Give the preparation type.
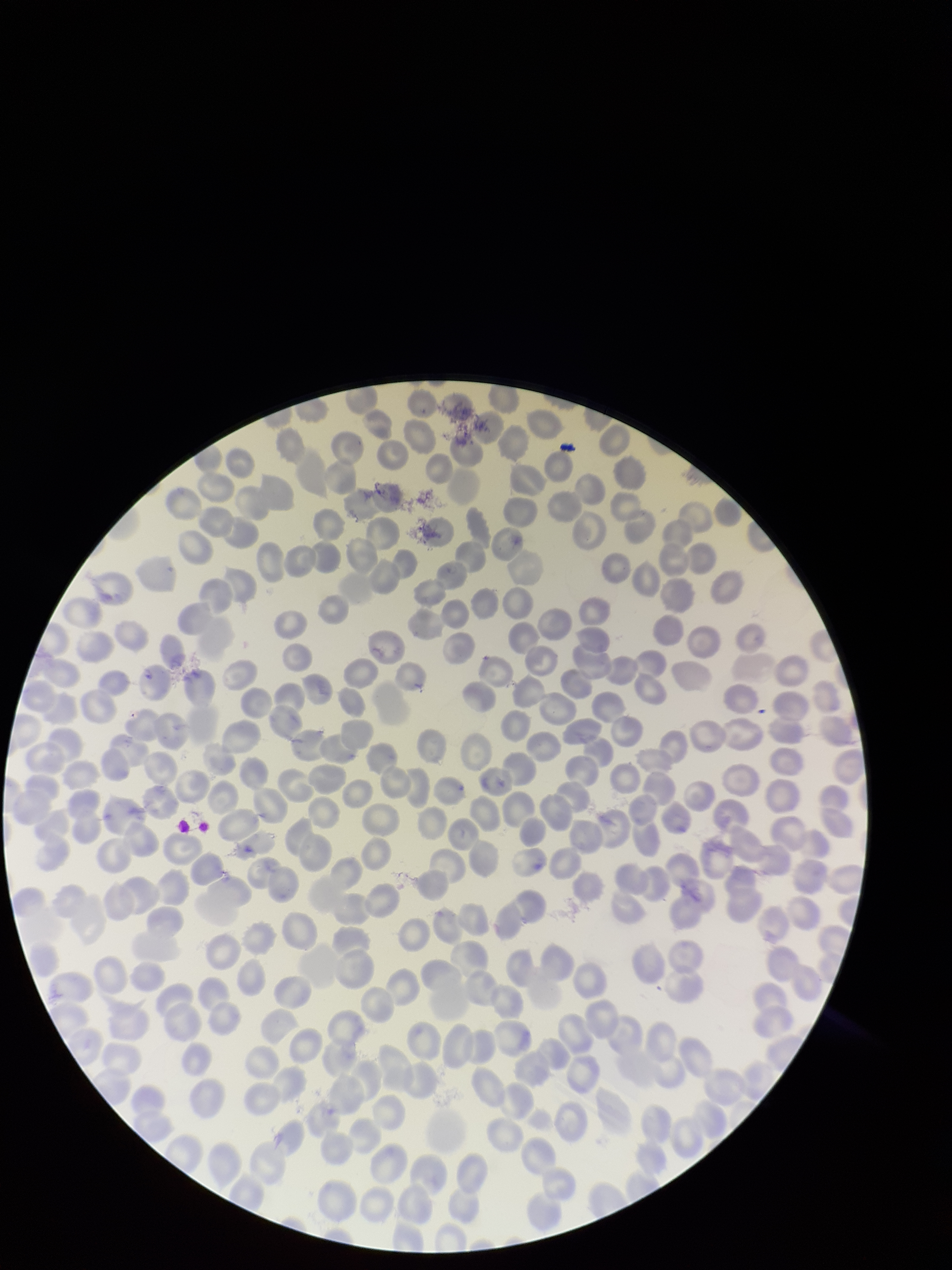
A thin smear.

Species reported for this patient: Plasmodium falciparum. Parasitized red blood cell count: 0. Red blood cell count: 235. Parasitized red blood cells: none seen. Single field of view. Photographed through the microscope eyepiece with a smartphone camera. Image is 952×1270 pixels. Stained with Giemsa. Patient malaria status: positive.